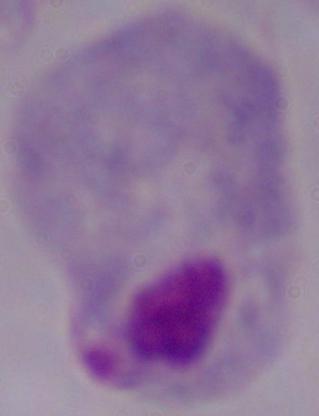

Summary:
  - Modality: micrograph
  - Magnification: 1000x
  - Identification: trichomonad